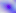
{
  "magnification": "400x",
  "modality": "photomicrograph",
  "identification": "Toxoplasma gondii"
}